Identify the blood parasite species.
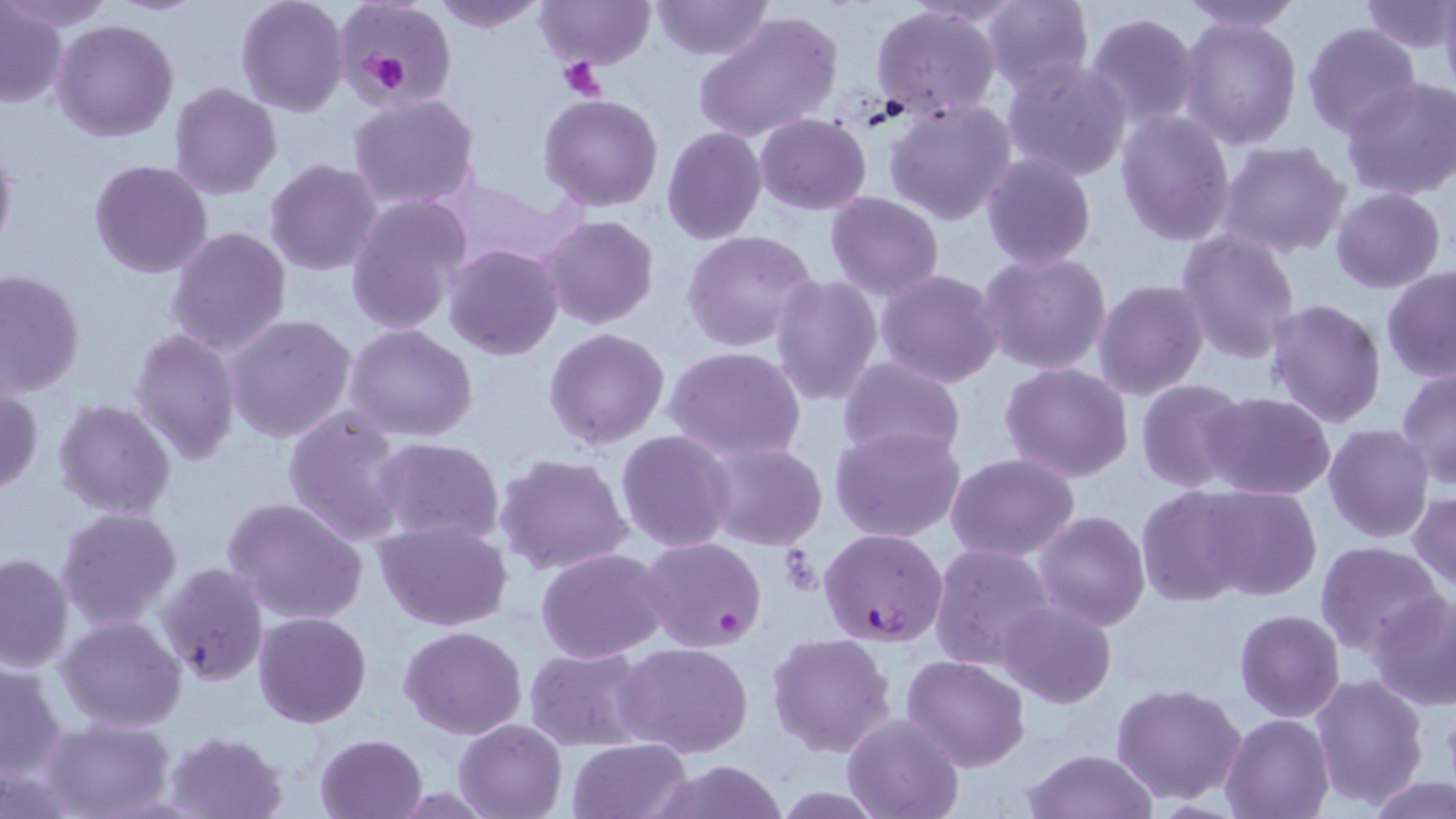
Plasmodium falciparum.

Summary:
  - Coordinate format: approximate bounding boxes as named x1/y1/x2/y2 corners in pixels
  - Uninfected red blood cell locations: (x1=5, y1=0, x2=113, y2=34), (x1=236, y1=0, x2=349, y2=117), (x1=332, y1=0, x2=457, y2=106), (x1=431, y1=0, x2=549, y2=32), (x1=535, y1=0, x2=654, y2=69), (x1=651, y1=0, x2=771, y2=60), (x1=1439, y1=0, x2=1456, y2=96), (x1=978, y1=1, x2=1095, y2=89), (x1=1180, y1=1, x2=1304, y2=33), (x1=1359, y1=2, x2=1455, y2=53), (x1=1, y1=5, x2=67, y2=109), (x1=871, y1=5, x2=1001, y2=118), (x1=694, y1=9, x2=843, y2=143), (x1=1083, y1=12, x2=1200, y2=131), (x1=1179, y1=17, x2=1303, y2=149), (x1=52, y1=18, x2=179, y2=141), (x1=1302, y1=21, x2=1420, y2=135), (x1=1001, y1=55, x2=1133, y2=183), (x1=1342, y1=76, x2=1456, y2=200), (x1=169, y1=84, x2=281, y2=200), (x1=346, y1=92, x2=481, y2=211), (x1=538, y1=93, x2=665, y2=211), (x1=885, y1=99, x2=1016, y2=226), (x1=1116, y1=109, x2=1236, y2=245), (x1=755, y1=113, x2=872, y2=214), (x1=661, y1=126, x2=768, y2=244), (x1=0, y1=141, x2=18, y2=260), (x1=1219, y1=141, x2=1350, y2=260), (x1=980, y1=153, x2=1097, y2=271), (x1=264, y1=158, x2=382, y2=277), (x1=88, y1=159, x2=214, y2=279), (x1=434, y1=179, x2=561, y2=272), (x1=1331, y1=188, x2=1445, y2=294), (x1=825, y1=192, x2=945, y2=301), (x1=344, y1=195, x2=471, y2=334), (x1=539, y1=215, x2=659, y2=330), (x1=165, y1=226, x2=292, y2=355), (x1=1175, y1=229, x2=1302, y2=362), (x1=681, y1=230, x2=817, y2=352), (x1=443, y1=243, x2=564, y2=363), (x1=979, y1=250, x2=1112, y2=375), (x1=1381, y1=267, x2=1455, y2=382), (x1=876, y1=268, x2=1004, y2=388), (x1=0, y1=269, x2=85, y2=397), (x1=770, y1=274, x2=883, y2=408), (x1=1095, y1=279, x2=1209, y2=401), (x1=1264, y1=299, x2=1387, y2=429), (x1=224, y1=313, x2=357, y2=444), (x1=345, y1=325, x2=477, y2=442), (x1=544, y1=327, x2=670, y2=449), (x1=131, y1=328, x2=241, y2=466), (x1=663, y1=346, x2=809, y2=462), (x1=838, y1=357, x2=965, y2=463), (x1=1000, y1=362, x2=1134, y2=482), (x1=1396, y1=365, x2=1456, y2=489), (x1=1136, y1=380, x2=1250, y2=492), (x1=0, y1=388, x2=43, y2=495), (x1=1199, y1=391, x2=1335, y2=498), (x1=52, y1=397, x2=178, y2=521), (x1=281, y1=405, x2=408, y2=544), (x1=1323, y1=424, x2=1434, y2=544), (x1=830, y1=426, x2=966, y2=543), (x1=616, y1=429, x2=737, y2=551), (x1=371, y1=437, x2=507, y2=549), (x1=700, y1=440, x2=829, y2=551), (x1=494, y1=453, x2=634, y2=577), (x1=945, y1=453, x2=1079, y2=561), (x1=1134, y1=484, x2=1256, y2=605), (x1=1197, y1=484, x2=1321, y2=600), (x1=1410, y1=490, x2=1456, y2=592), (x1=221, y1=494, x2=370, y2=627), (x1=55, y1=505, x2=182, y2=630), (x1=1033, y1=511, x2=1151, y2=631), (x1=373, y1=519, x2=515, y2=633), (x1=934, y1=529, x2=1156, y2=653), (x1=637, y1=536, x2=767, y2=655), (x1=1315, y1=540, x2=1444, y2=657), (x1=930, y1=543, x2=1055, y2=671), (x1=535, y1=547, x2=671, y2=662), (x1=0, y1=553, x2=74, y2=671), (x1=156, y1=562, x2=268, y2=686), (x1=1364, y1=588, x2=1456, y2=710), (x1=997, y1=600, x2=1117, y2=709), (x1=1235, y1=609, x2=1345, y2=721), (x1=253, y1=611, x2=373, y2=729), (x1=57, y1=615, x2=187, y2=733), (x1=399, y1=625, x2=527, y2=739), (x1=767, y1=632, x2=897, y2=757), (x1=614, y1=641, x2=753, y2=756), (x1=523, y1=645, x2=652, y2=750), (x1=902, y1=655, x2=1029, y2=771), (x1=1, y1=660, x2=69, y2=779), (x1=1312, y1=674, x2=1429, y2=809), (x1=1111, y1=681, x2=1246, y2=805), (x1=842, y1=713, x2=963, y2=819), (x1=1221, y1=713, x2=1333, y2=819), (x1=39, y1=717, x2=176, y2=819), (x1=454, y1=718, x2=566, y2=819), (x1=164, y1=730, x2=290, y2=819), (x1=314, y1=733, x2=429, y2=819), (x1=567, y1=738, x2=694, y2=819), (x1=1020, y1=749, x2=1158, y2=819), (x1=651, y1=761, x2=788, y2=818), (x1=1369, y1=776, x2=1455, y2=819)
  - Platelet locations: (x1=350, y1=40, x2=420, y2=97), (x1=556, y1=57, x2=607, y2=101)
  - Plasmodium falciparum-infected red blood cell locations: (x1=818, y1=527, x2=948, y2=646)
  - Magnification: 1000x
  - Image size: 1456×819 pixels
  - Modality: optical microscopy
  - Stain: May-Grünwald-Giemsa
  - Field of view: one of a larger specimen
  - Preparation: thin blood smear